Classify the preparation.
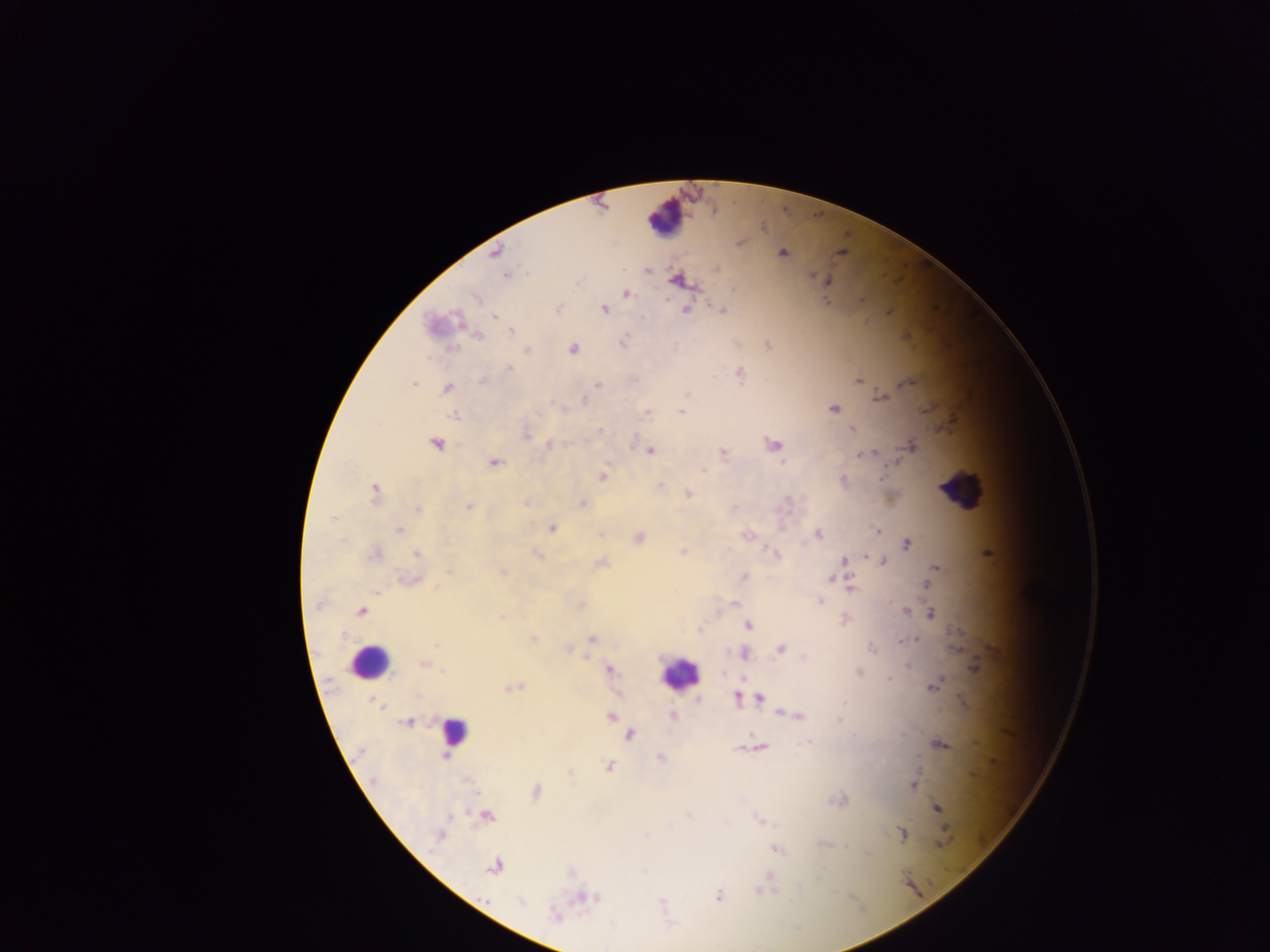
Thick blood film.

Approximate centers as x y in pixels.
Summary:
  - Leukocyte locations: 665 217; 962 489; 369 661; 678 673; 453 732
  - Plasmodium parasite locations: 496 252; 841 252; 782 253; 717 268; 648 271; 506 274; 814 275; 676 280; 827 281; 626 293; 475 298; 826 303; 559 308; 686 308; 604 309; 721 310; 494 316; 642 318; 511 331; 479 336; 623 342; 572 349; 527 350; 509 368; 740 374; 859 380; 482 381; 414 383; 910 383; 599 385; 447 388; 687 394; 881 397; 584 401; 834 409; 681 411; 647 413; 455 415; 852 428; 600 430; 526 436; 436 444; 549 444; 774 445; 911 446; 649 451; 863 453; 723 454; 871 454; 783 462; 495 463; 702 470; 603 476; 882 477; 844 479; 659 485; 375 493; 688 494; 582 503; 469 508; 734 508; 417 509; 333 518; 552 528; 399 530; 878 531; 818 534; 600 535; 638 538; 907 544; 683 552; 375 553; 417 554; 775 554; 539 556; 865 556; 845 559; 602 562; 883 562; 935 567; 448 572; 503 572; 744 576; 831 579; 408 580; 925 584; 852 588; 376 592; 820 601; 735 603; 581 605; 317 606; 362 611; 906 611; 932 613; 501 618; 749 625; 700 630; 535 638; 916 638; 591 639; 900 641; 436 645; 871 648; 780 650; 744 654; 424 665; 907 666; 974 666; 610 670; 443 672; 889 679; 933 687; 516 688; 417 697; 736 697; 699 699; 760 699; 845 703; 796 716; 611 717; 672 717; 839 720; 409 722; 630 735; 522 739; 940 745; 740 748; 761 748; 444 755; 660 758; 608 766; 570 772; 467 780; 913 785; 536 791; 936 807; 687 815; 450 816; 488 817; 762 821; 946 831; 903 834; 439 835; 941 843; 777 849; 494 867; 761 891; 718 896; 589 898; 520 902; 553 914
  - Country: Ghana
  - Capture: mobile-phone photograph through a microscope
  - Image size: 1270×952 pixels
  - Field of view: single